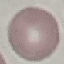
Summary:
  - Malaria status: uninfected
  - Stain: Giemsa
  - Preparation: thin blood smear
  - Capture: smartphone camera at the microscope eyepiece
  - Image type: cell patch, automatically extracted from a larger field of view and resized to 64 × 64 pixels